Assess this cell for malaria.
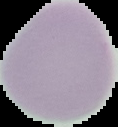
Uninfected.

{
  "preparation": "thin blood smear",
  "image_size": "118×127 pixels",
  "image_type": "segmented cell region with the area outside set to black"
}